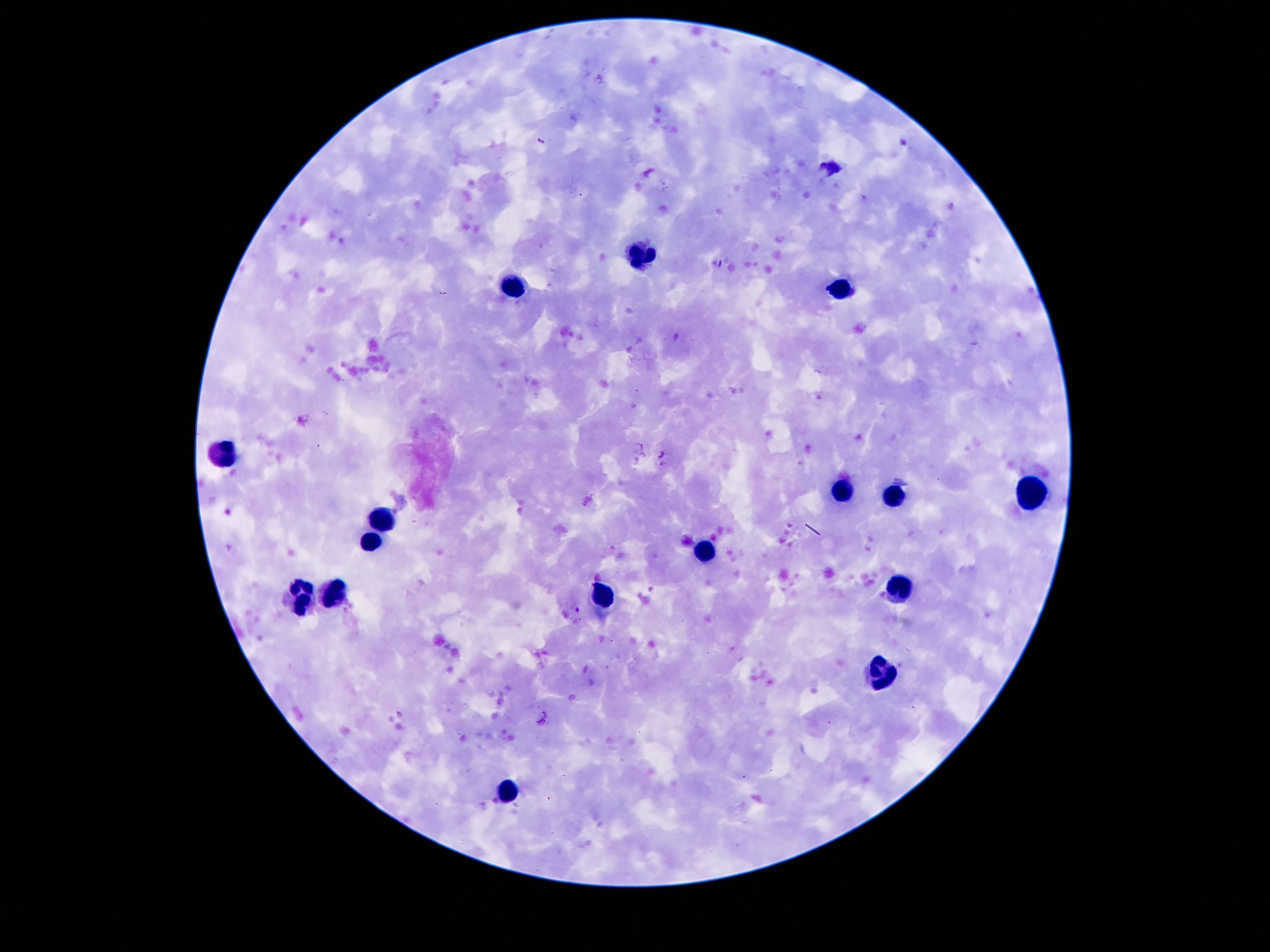
Approximate object centers, in pixels from the top-left corner.
Summary:
  - Leukocyte locations: (x=636, y=254), (x=512, y=281), (x=836, y=289), (x=223, y=449), (x=1031, y=486), (x=843, y=489), (x=893, y=494), (x=381, y=516), (x=371, y=536), (x=707, y=548), (x=900, y=588), (x=332, y=593), (x=604, y=593), (x=302, y=598), (x=880, y=674), (x=510, y=788)
  - Image size: 1270×952 pixels
  - Preparation: thick blood film
  - Stain: Giemsa
  - Magnification: 100x
  - Field of view: one from this slide
  - Patient malaria status: negative
  - Capture: smartphone camera through the microscope eyepiece